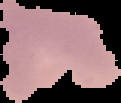

Summary:
  - Image type: segmented cell region with the area outside set to black
  - Image size: 121×103 pixels
  - Preparation: thin blood film
  - Malaria status: parasitized